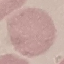

malaria_status: uninfected
image_type: automatically extracted cell patch, resized to 64 × 64 pixels
capture: smartphone camera at the microscope eyepiece
stain: Giemsa
preparation: thin blood film